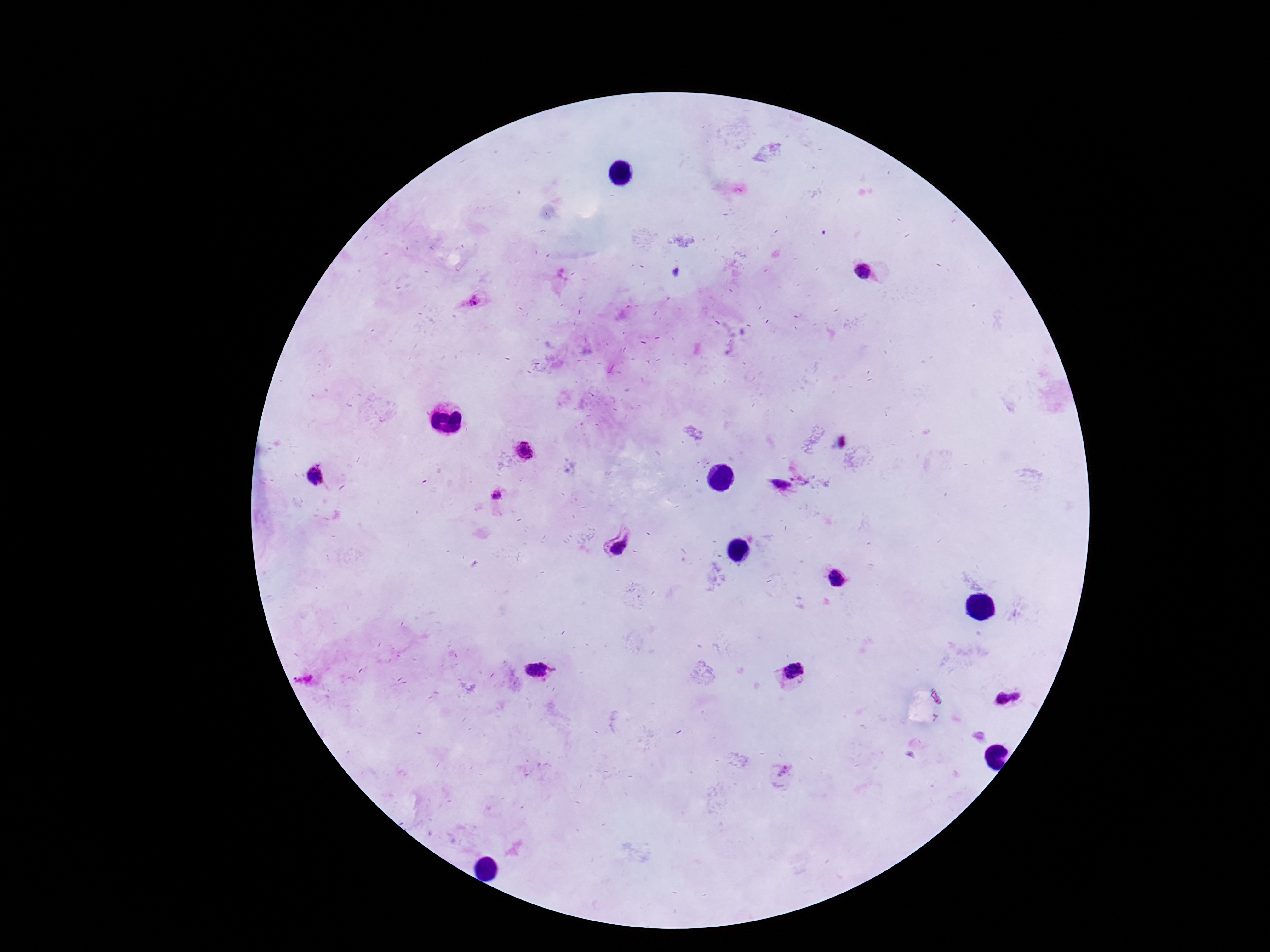
Approximate centers as {x, y} in pixels.
Summary:
  - Plasmodium parasite locations: {862, 271}, {472, 302}, {524, 450}, {314, 477}, {780, 485}, {497, 495}, {619, 541}, {837, 580}, {538, 671}, {792, 672}, {1009, 698}
  - Capture: smartphone camera through the microscope eyepiece
  - Preparation: thick peripheral-blood smear
  - Magnification: 100x
  - Stain: Giemsa
  - Patient malaria status: positive
  - Field of view: one from this slide
  - Image size: 1270×952 pixels